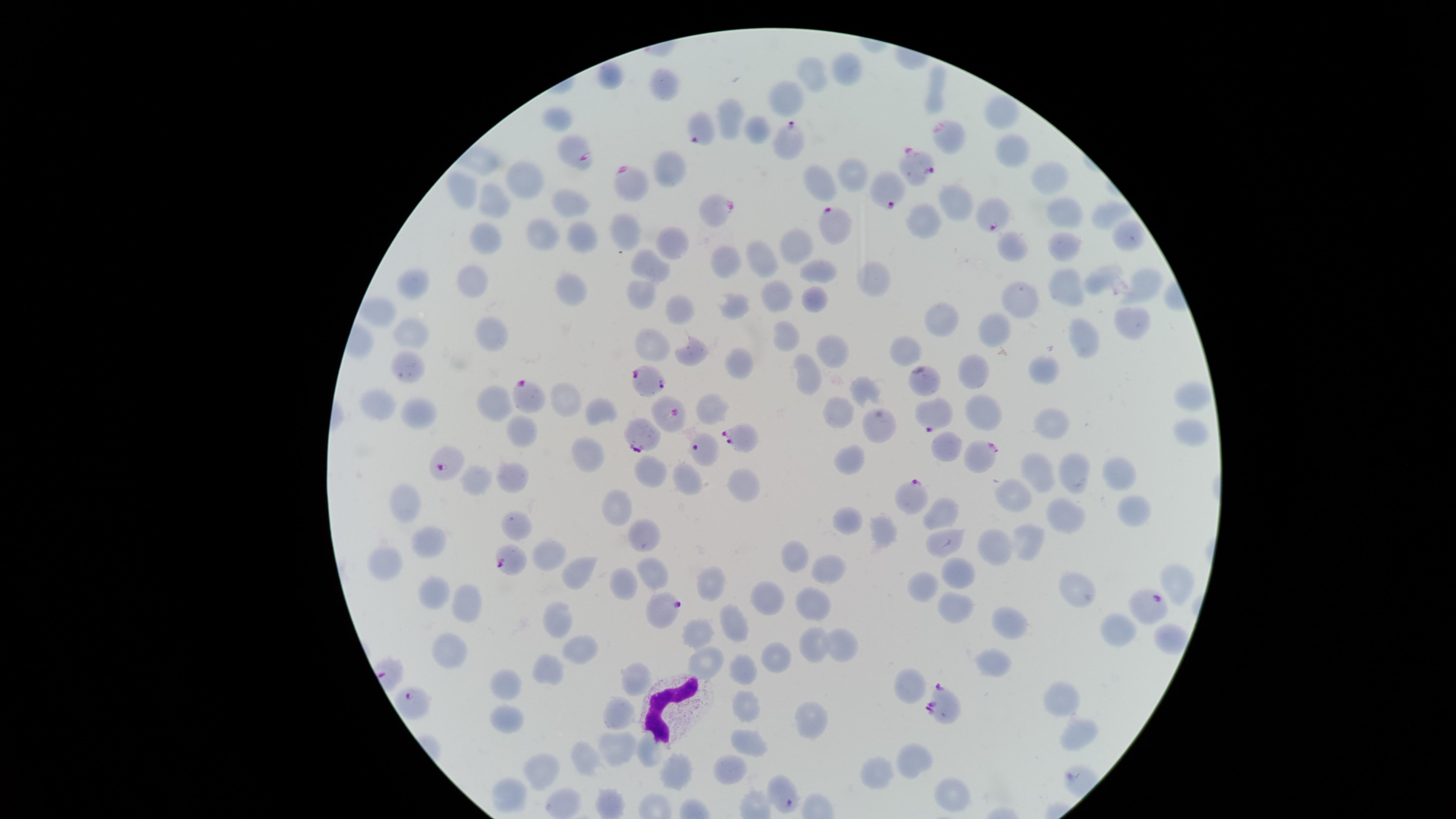

species = Plasmodium falciparum
capture = smartphone photograph through the microscope eyepiece
white blood cells = approximate marker points as [x, y] in pixels: [662, 706]
parasitized red blood cells = approximate marker points as [x, y] in pixels: [704, 131], [946, 132], [789, 136], [573, 152], [922, 169], [627, 183], [891, 190], [716, 214], [988, 216], [831, 222], [647, 376], [920, 377], [530, 399], [937, 410], [674, 414], [641, 434], [745, 435], [700, 449], [984, 458], [446, 460], [909, 493], [508, 562], [1152, 605], [665, 608], [410, 702], [937, 705]
image size = 1456×819 pixels
presence = malaria parasites identified
preparation = thin blood smear
uninfected red blood cells = approximate marker points as [x, y] in pixels: [844, 70], [608, 74], [811, 74], [662, 86], [933, 97], [784, 100], [1001, 111], [734, 113], [553, 120], [758, 124], [1015, 151], [671, 169], [1051, 176], [853, 177], [531, 178], [821, 183], [467, 188], [954, 199], [571, 200], [495, 203], [1107, 211], [1062, 213], [927, 223], [628, 228], [542, 232], [1128, 233], [486, 237], [582, 237], [1019, 241], [672, 242], [1070, 244], [795, 248], [768, 255], [725, 257], [654, 265], [819, 274], [471, 279], [1101, 279], [874, 280], [417, 284], [1067, 285], [641, 288], [568, 291], [1142, 291], [778, 294], [816, 297], [1025, 299], [737, 304], [676, 310], [381, 312], [944, 321], [1134, 322], [996, 326], [490, 334], [414, 336], [788, 337], [1083, 339], [649, 345], [833, 350], [906, 350], [699, 356], [739, 359], [408, 365], [803, 371], [973, 371], [1043, 372], [859, 388], [1191, 392], [566, 399], [380, 403], [492, 407], [598, 412], [417, 413], [833, 416], [982, 416], [1052, 422], [884, 425], [1186, 430], [524, 431], [586, 456], [844, 461], [1117, 469], [1041, 471], [1072, 471], [649, 473], [687, 475], [739, 478], [471, 479], [510, 479], [405, 494], [1011, 494], [617, 507], [1130, 512], [945, 514], [846, 515], [1066, 518], [517, 526], [882, 534], [956, 534], [644, 535], [1029, 538], [426, 540], [995, 544], [543, 556], [794, 558], [387, 562], [575, 571], [650, 571], [958, 573], [825, 578], [1177, 581], [621, 583], [926, 585], [711, 587], [1076, 590], [438, 595], [769, 598], [465, 602], [809, 603], [955, 609], [1010, 620], [555, 622], [735, 626], [1117, 626], [701, 632], [1165, 641], [818, 642], [845, 646], [581, 649], [449, 654], [994, 661], [774, 662], [706, 663], [745, 671], [546, 673], [634, 676], [507, 679], [911, 687], [1062, 700], [617, 706], [745, 707], [499, 715], [811, 720], [1075, 736], [748, 737], [615, 749], [652, 754], [588, 758], [917, 759], [730, 767], [542, 768], [674, 770], [878, 771], [947, 789], [511, 797], [551, 807]
visible region = circular
field of view = single
stain = Giemsa